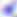
modality = photomicrograph
identification = Toxoplasma gondii
magnification = 400x